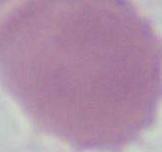
modality = photomicrograph
identification = red blood cell
magnification = 1000x